Give the position of every malaria parasite.
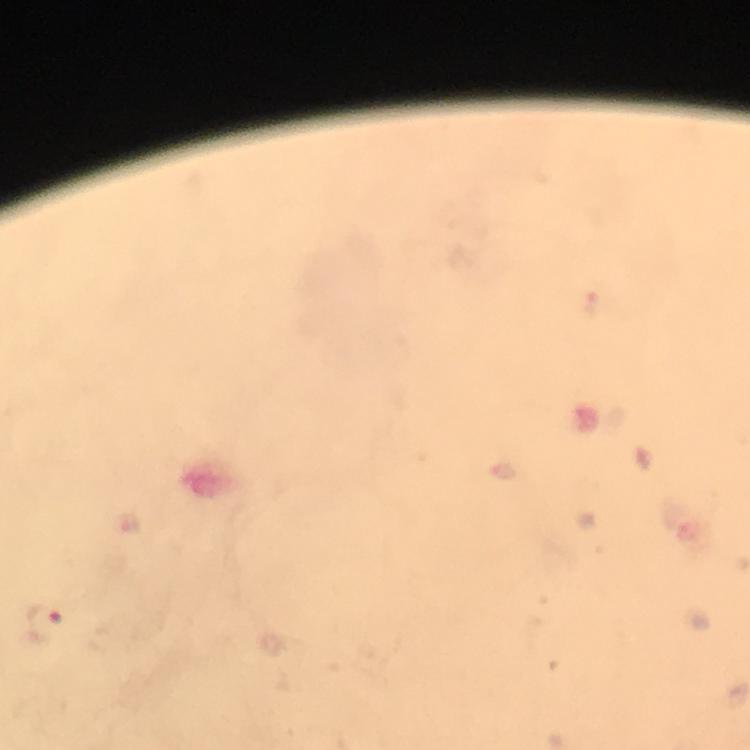

Approximate centers as {x, y} in pixels.
Malaria parasites: {44, 622}.

Summary:
  - Capture: smartphone photograph through a microscope
  - Context: from a malaria diagnostic workup
  - Stain: Giemsa
  - Cropped from: a single field of view
  - Magnification: 100x
  - Image size: 750×750 pixels
  - Preparation: thick blood smear
  - Immersion oil: used